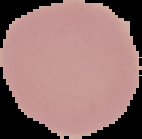
preparation = thin blood smear
result = negative for malaria parasites
image size = 142×139 pixels
image type = segmented cell region on a black background